Locate every blood parasite and identify its species.
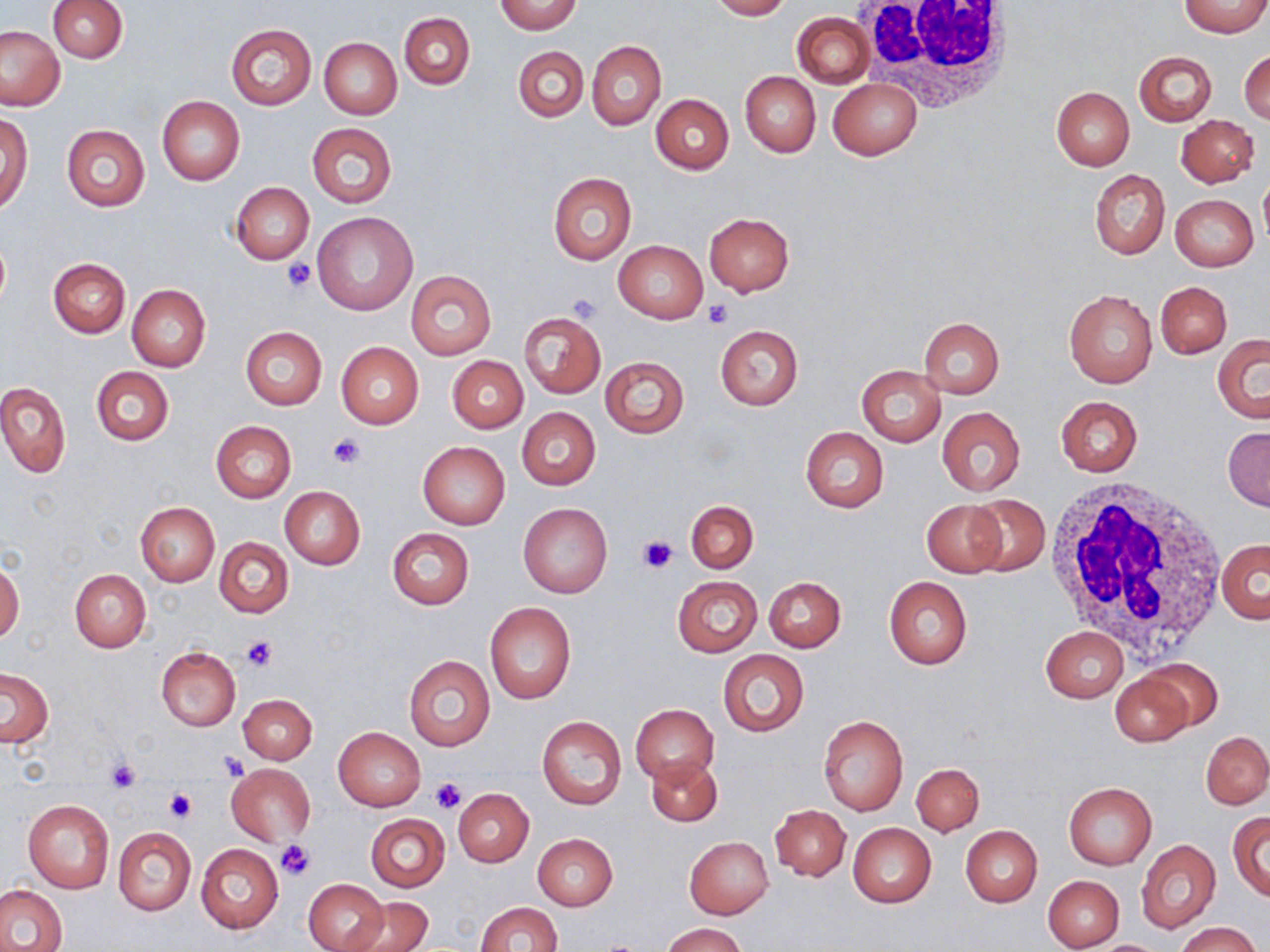
No blood parasites observed.

slide-level diagnosis = negative for blood parasites
stain = May-Grünwald-Giemsa
field of view = single
white blood cell locations = approximate bounding boxes as (x1, y1, x2, y2) in pixels: (852, 0, 1020, 107), (1041, 473, 1228, 657)
uninfected red blood cell locations = approximate bounding boxes as (x1, y1, x2, y2) in pixels: (496, 0, 580, 34), (709, 0, 792, 20), (47, 1, 127, 63), (1180, 1, 1268, 37), (400, 12, 475, 90), (793, 13, 874, 87), (226, 24, 316, 109), (1, 25, 66, 111), (319, 37, 402, 120), (587, 41, 665, 129), (513, 46, 588, 122), (1240, 49, 1269, 127), (1134, 50, 1217, 127), (741, 72, 820, 158), (828, 79, 922, 160), (1051, 86, 1134, 169), (651, 93, 734, 173), (157, 96, 245, 185), (1176, 114, 1259, 187), (0, 115, 32, 213), (306, 122, 396, 208), (61, 123, 150, 212), (1089, 169, 1169, 260), (1259, 172, 1270, 246), (548, 173, 636, 265), (231, 182, 314, 263), (1170, 194, 1259, 271), (312, 211, 419, 316), (704, 213, 794, 296), (0, 236, 10, 312), (613, 240, 708, 323), (49, 257, 130, 338), (406, 271, 495, 358), (1155, 282, 1231, 357), (126, 284, 212, 371), (1064, 289, 1157, 388), (518, 312, 606, 399), (918, 317, 1005, 398), (717, 326, 802, 410), (240, 327, 327, 410), (1212, 335, 1270, 422), (336, 341, 424, 429), (447, 355, 528, 434), (599, 356, 689, 438), (856, 365, 945, 447), (90, 367, 174, 446), (0, 382, 71, 478), (1055, 396, 1142, 477), (937, 407, 1025, 496), (517, 408, 600, 489), (211, 421, 296, 502), (1223, 426, 1269, 511), (801, 427, 888, 514), (418, 441, 509, 530), (280, 486, 365, 570), (964, 494, 1050, 575), (921, 500, 1007, 577), (685, 501, 758, 572), (135, 502, 218, 586), (519, 503, 613, 598), (387, 527, 474, 609), (214, 537, 294, 618), (1216, 538, 1268, 624), (0, 560, 24, 644), (68, 568, 151, 652), (673, 576, 762, 657), (763, 576, 846, 652), (883, 576, 972, 670), (484, 603, 576, 705), (1040, 626, 1128, 702), (156, 647, 240, 730), (718, 650, 809, 737), (403, 654, 494, 752), (1140, 657, 1225, 733), (1, 668, 53, 747), (1110, 672, 1193, 747), (236, 694, 317, 763), (630, 703, 718, 785), (818, 714, 908, 816), (537, 716, 627, 811), (333, 726, 426, 811), (1201, 731, 1270, 810), (647, 755, 722, 826), (912, 763, 984, 836), (227, 764, 316, 847), (1066, 781, 1156, 868), (453, 788, 534, 866), (22, 798, 113, 893), (770, 804, 851, 882), (1229, 812, 1270, 900), (365, 813, 450, 893), (848, 822, 936, 909), (960, 825, 1043, 907), (114, 827, 195, 915), (533, 833, 618, 911), (684, 836, 774, 919), (1137, 840, 1220, 933), (196, 844, 283, 932), (1043, 875, 1123, 950), (303, 879, 389, 952), (0, 885, 67, 952), (349, 897, 432, 952), (474, 902, 562, 952), (660, 922, 746, 952), (1174, 922, 1263, 952), (1082, 939, 1172, 951)
magnification = 1000x
modality = light microscopy
preparation = thin blood smear
image size = 1270×952 pixels
platelet locations = approximate bounding boxes as (x1, y1, x2, y2) in pixels: (281, 257, 317, 293), (566, 293, 601, 322), (703, 298, 733, 329), (326, 430, 367, 468), (637, 535, 677, 574), (240, 637, 277, 672), (218, 750, 250, 780), (106, 759, 142, 793), (430, 776, 465, 814), (164, 787, 195, 822), (275, 841, 316, 883)